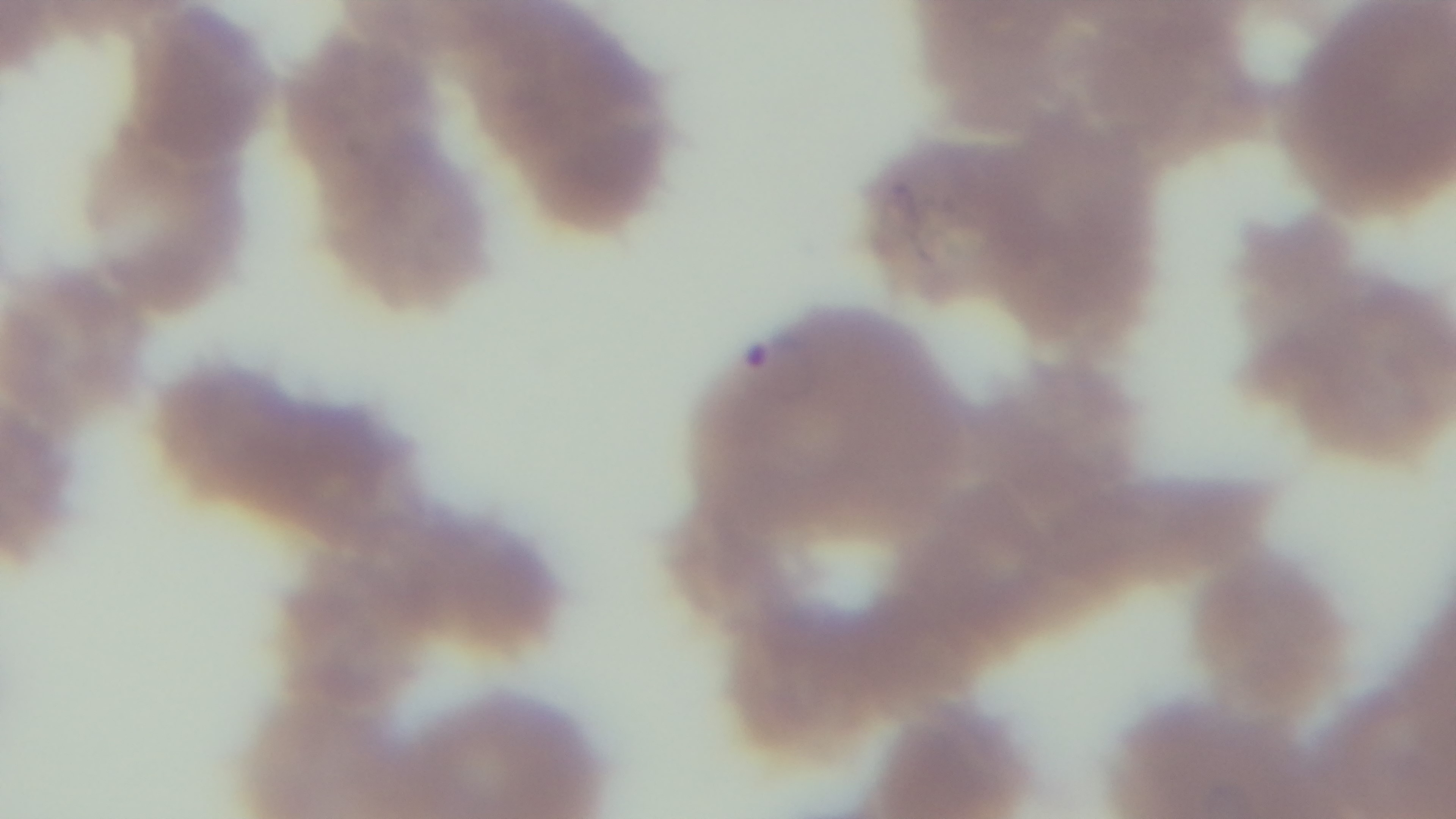
100x oil-immersion objective. Light microscopy. Preparation: thin. Giemsa stain. Malaria status: infected. One field from the slide. Mounted 4K digital camera.